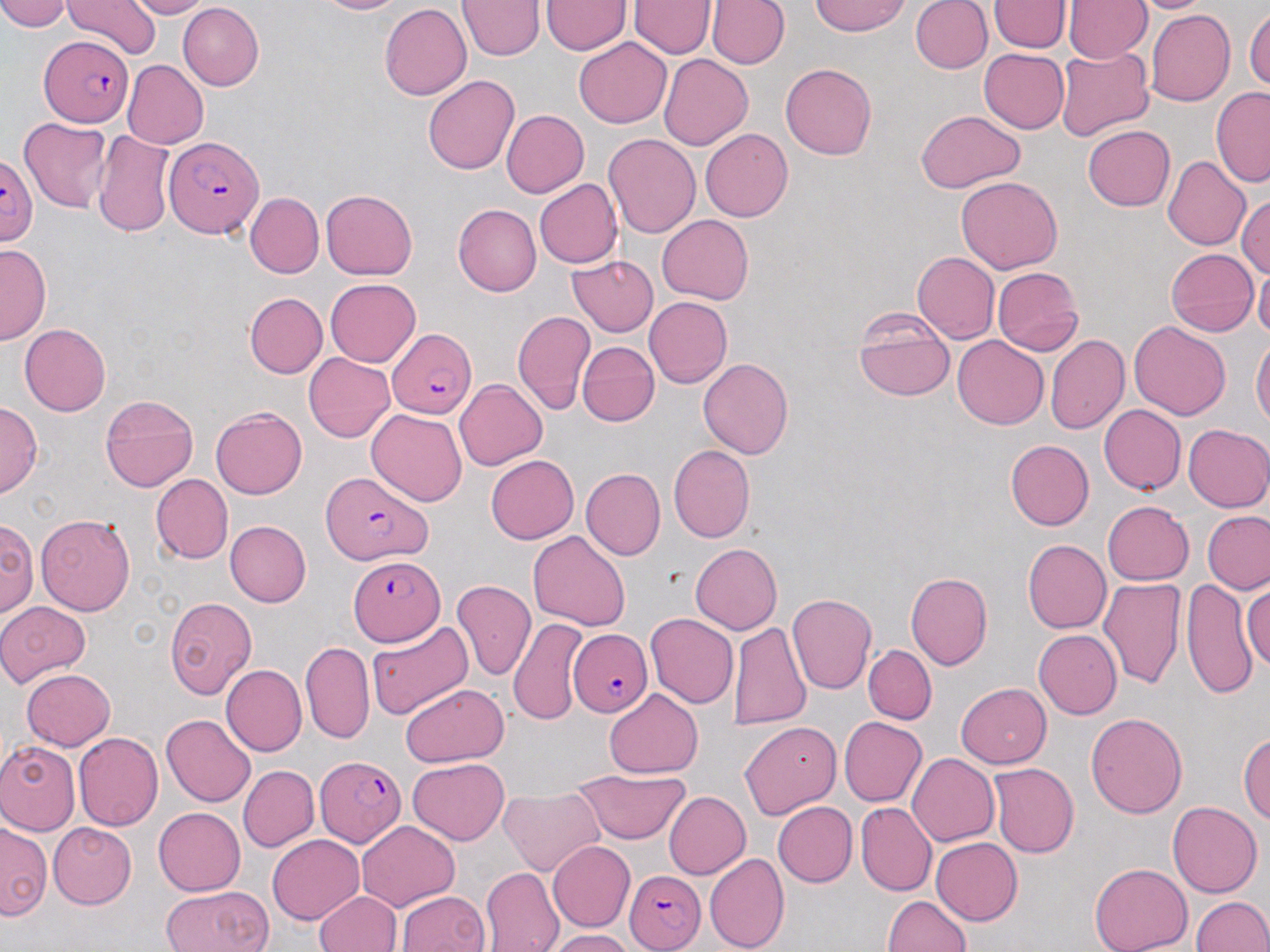

Summary:
  - Coordinate format: approximate bounding boxes as [x1, y1, x2, y2] in pixels
  - Plasmodium falciparum-infected red blood cell locations: [40, 35, 133, 128], [164, 135, 264, 238], [0, 155, 38, 246], [389, 331, 474, 420], [320, 468, 431, 566], [349, 555, 446, 645], [568, 629, 653, 717], [316, 755, 405, 847], [625, 869, 706, 950]
  - Uninfected red blood cell locations: [0, 0, 73, 32], [64, 0, 161, 60], [123, 0, 211, 19], [311, 0, 405, 14], [542, 0, 632, 54], [911, 0, 992, 74], [989, 0, 1072, 53], [1127, 0, 1215, 13], [457, 1, 544, 60], [630, 1, 715, 57], [707, 1, 790, 69], [811, 1, 911, 36], [1064, 1, 1151, 64], [178, 3, 263, 90], [380, 4, 472, 100], [1244, 7, 1270, 93], [1145, 10, 1236, 107], [574, 37, 672, 128], [1055, 46, 1154, 140], [978, 48, 1069, 133], [659, 53, 752, 150], [122, 59, 208, 149], [780, 62, 876, 160], [422, 74, 519, 175], [1211, 87, 1270, 188], [501, 109, 588, 198], [917, 110, 1025, 194], [19, 117, 113, 214], [1083, 125, 1175, 211], [700, 128, 793, 222], [93, 131, 174, 237], [604, 134, 700, 238], [1163, 156, 1251, 250], [956, 176, 1063, 274], [534, 178, 622, 268], [321, 190, 417, 279], [1236, 192, 1270, 280], [245, 193, 323, 278], [457, 197, 623, 286], [452, 204, 541, 296], [657, 214, 753, 304], [0, 244, 51, 344], [1165, 247, 1259, 336], [912, 252, 1000, 343], [567, 255, 659, 336], [1254, 261, 1270, 343], [991, 266, 1083, 356], [325, 278, 421, 367], [244, 292, 327, 377], [644, 297, 732, 388], [853, 308, 955, 401], [512, 310, 595, 415], [1129, 321, 1231, 420], [20, 324, 111, 416], [953, 335, 1048, 429], [1045, 335, 1129, 435], [1251, 336, 1270, 429], [577, 341, 659, 426], [304, 353, 394, 441], [698, 359, 795, 459], [454, 379, 548, 471], [99, 392, 198, 492], [0, 402, 41, 496], [1099, 404, 1186, 494], [211, 406, 307, 500], [368, 408, 467, 506], [1182, 424, 1270, 512], [1005, 440, 1094, 531], [668, 445, 756, 543], [486, 455, 579, 543], [580, 468, 666, 559], [151, 474, 233, 563], [1102, 501, 1194, 585], [1202, 510, 1270, 594], [35, 514, 136, 616], [2, 516, 39, 616], [225, 520, 311, 607], [528, 530, 630, 631], [1022, 540, 1111, 633], [690, 543, 781, 634], [906, 572, 992, 671], [1099, 576, 1187, 690], [1181, 576, 1257, 702], [453, 579, 536, 681], [1243, 584, 1270, 671], [786, 592, 876, 694], [164, 596, 257, 700], [0, 601, 90, 686], [645, 613, 739, 708], [509, 617, 589, 724], [366, 620, 474, 721], [730, 622, 810, 731], [1034, 630, 1122, 718], [300, 641, 374, 745], [863, 645, 937, 724], [220, 665, 306, 757], [21, 669, 114, 751], [956, 683, 1052, 768], [400, 684, 509, 765], [604, 689, 702, 778], [1086, 713, 1188, 819], [161, 715, 256, 807], [839, 717, 927, 806], [740, 721, 841, 818], [73, 732, 163, 831], [1238, 732, 1269, 823], [0, 741, 80, 835], [908, 753, 1000, 846], [407, 757, 508, 845], [988, 762, 1079, 858], [238, 764, 319, 852], [572, 768, 689, 844], [499, 788, 603, 877], [663, 790, 750, 879], [772, 801, 857, 887], [1168, 801, 1262, 898], [856, 802, 937, 896], [154, 807, 246, 896], [355, 820, 459, 911], [0, 822, 52, 920], [47, 822, 137, 909], [266, 835, 363, 924], [931, 838, 1022, 925], [548, 841, 635, 932], [704, 852, 790, 952], [1089, 863, 1193, 952], [481, 866, 565, 952], [161, 885, 271, 951], [397, 890, 489, 952], [314, 891, 402, 952], [883, 895, 971, 952], [1192, 896, 1269, 951], [547, 929, 633, 952]
  - Slide-level diagnosis: Plasmodium falciparum
  - Preparation: thin blood smear
  - Modality: optical microscopy
  - Field of view: single
  - Magnification: 1000x
  - Image size: 1270×952 pixels
  - Stain: May-Grünwald-Giemsa